Describe the morphology of the erythrocytes.
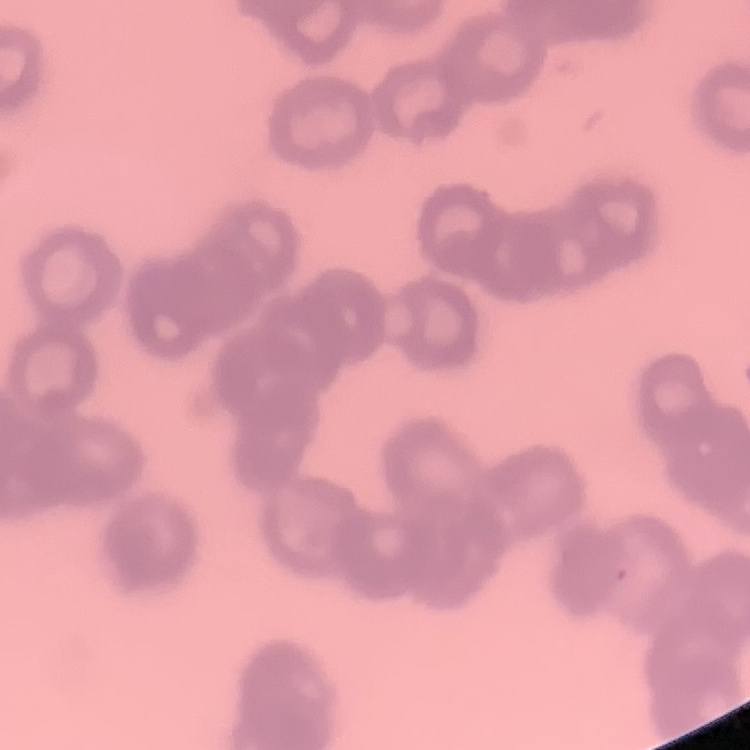
Rouleaux formation.

preparation = thin peripheral smear
stain = Field's or Giemsa
image type = square crop of a larger photomicrograph